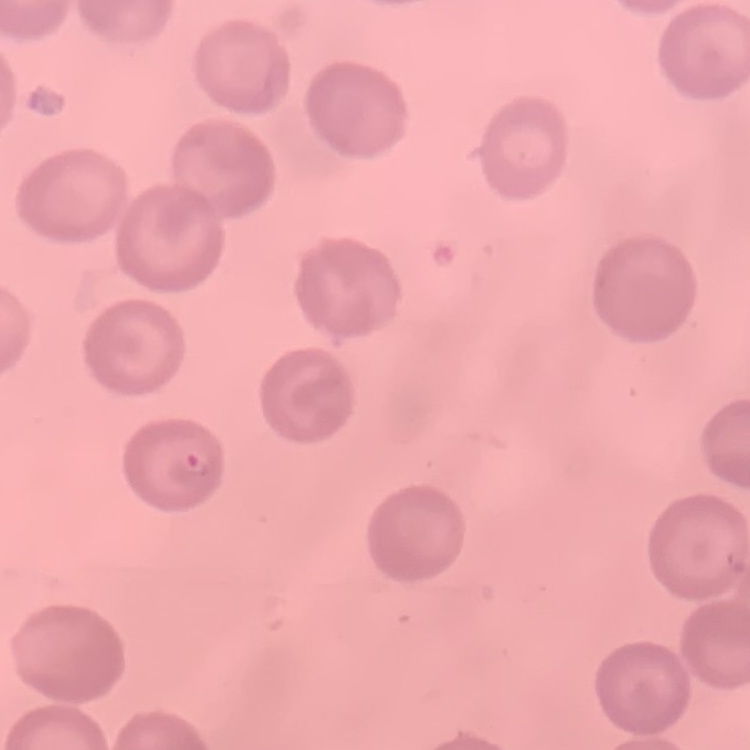

Summary:
  - Red blood cell morphology: no rouleaux formation
  - Stain: Field's or Giemsa
  - Image type: one tile cut from a larger photomicrograph
  - Preparation: thin blood smear